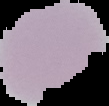
image_type: segmented cell region on a black background
preparation: thin blood film
malaria_status: uninfected
image_size: 109×106 pixels